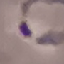
Malaria status: parasitized. Thin blood film. Acquired by smartphone through the microscope eyepiece. Automatically extracted cell patch, resized to 64 × 64 pixels. Giemsa-stained preparation.